Identify the parasite.
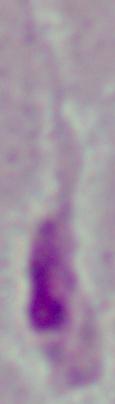
Leishmania.

Photomicrograph. Captured at 1000x magnification.